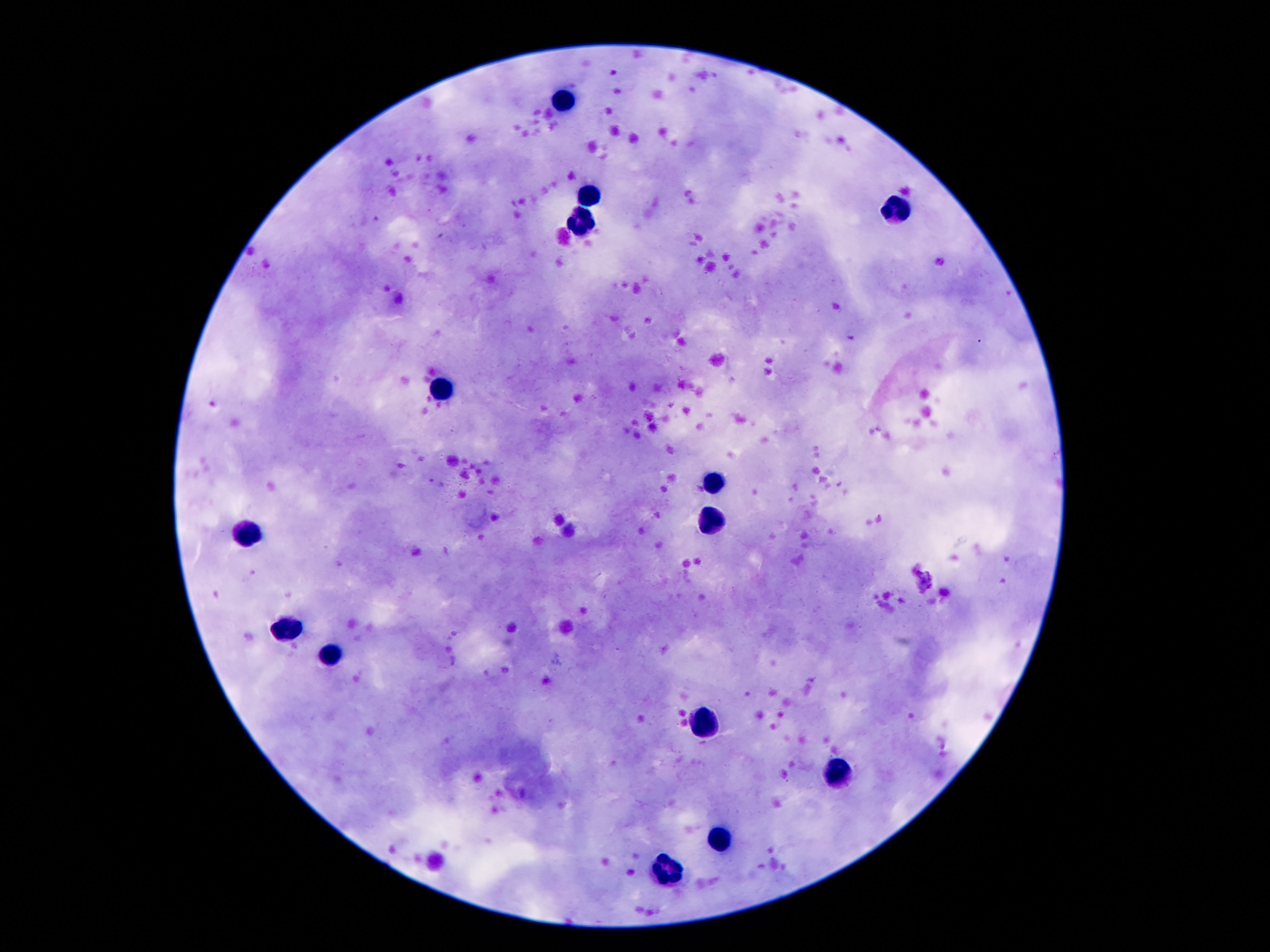 Approximate centers as (x, y) in pixels. Leukocyte locations: (563, 100), (590, 197), (897, 209), (584, 222), (438, 384), (713, 481), (711, 520), (245, 533), (288, 628), (329, 655), (706, 722), (838, 775), (722, 837), (668, 869). 100x magnification. Image is 1270×952 pixels. Smartphone photograph taken through the microscope eyepiece. Patient malaria status: uninfected. Thick blood smear. Giemsa stain. Single field of view.